Draw a bounding box around every malaria parasite, every leukocyte, and every artifact (stain precipitate or debris).
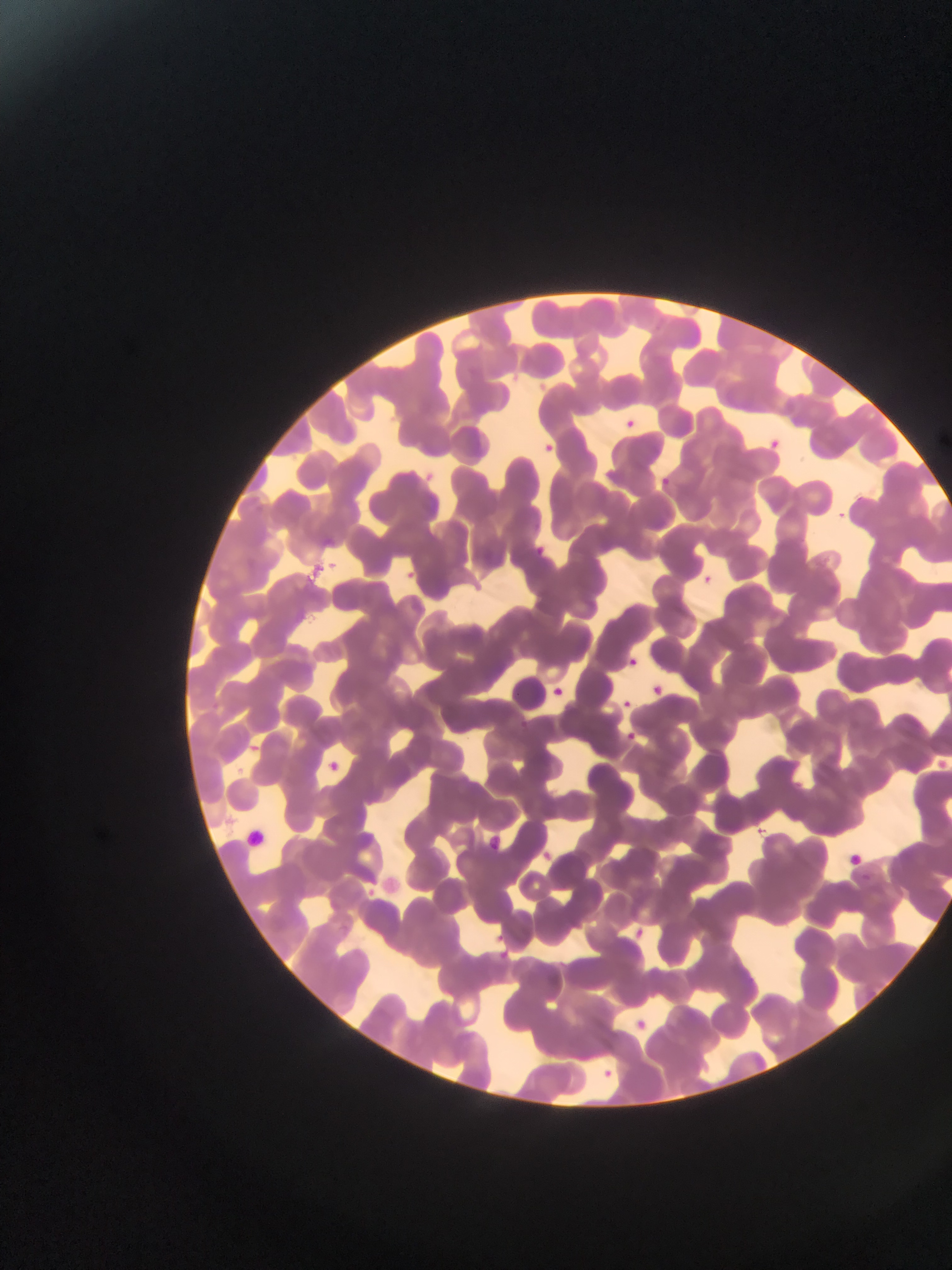

Approximate bounding boxes as [left, top, right, bottom] in pixels.
No malaria parasites observed.
Leukocytes: [240, 824, 270, 854].

{
  "preparation": "thin blood smear",
  "field_of_view": "single",
  "image_size": "952×1270 pixels",
  "capture": "mobile-phone photograph through a microscope",
  "country": "Ghana"
}